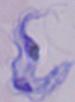

1000x magnification. A trypanosome is seen. Micrograph.